Assess this cell for malaria.
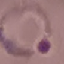

It is parasitized.

Thin smear of blood. Cell patch, automatically extracted from a larger field of view and resized to 64 × 64 pixels. Photographed with a smartphone camera at the microscope eyepiece. Giemsa stain.